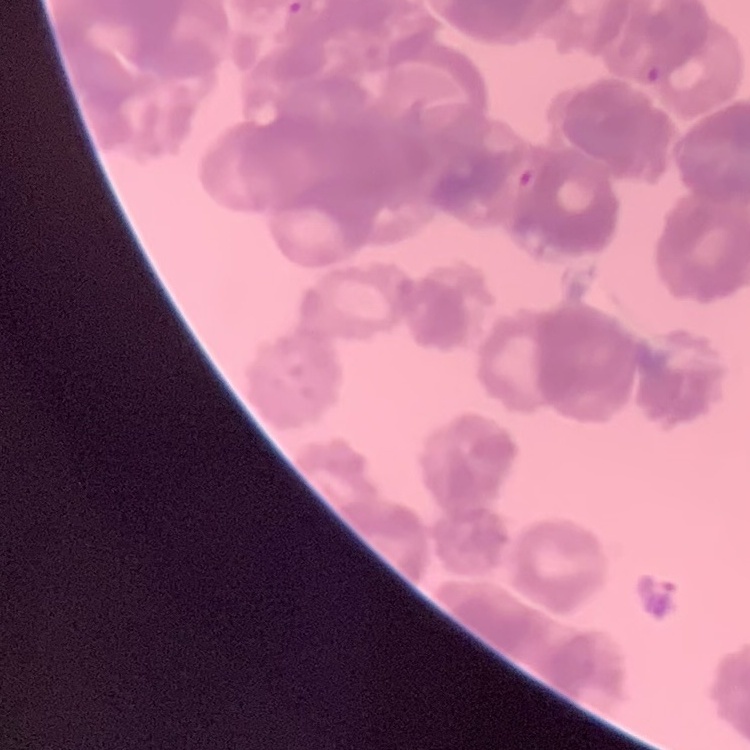
The red blood cells exhibit rouleaux formation. Thin peripheral smear. Field's or Giemsa stain. One tile cut from a larger photomicrograph.